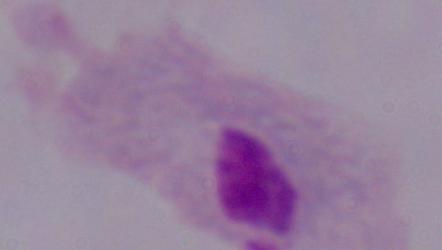

Summary:
  - Identification: trichomonad
  - Modality: micrograph
  - Magnification: 1000x